Locate every leukocyte (white blood cell).
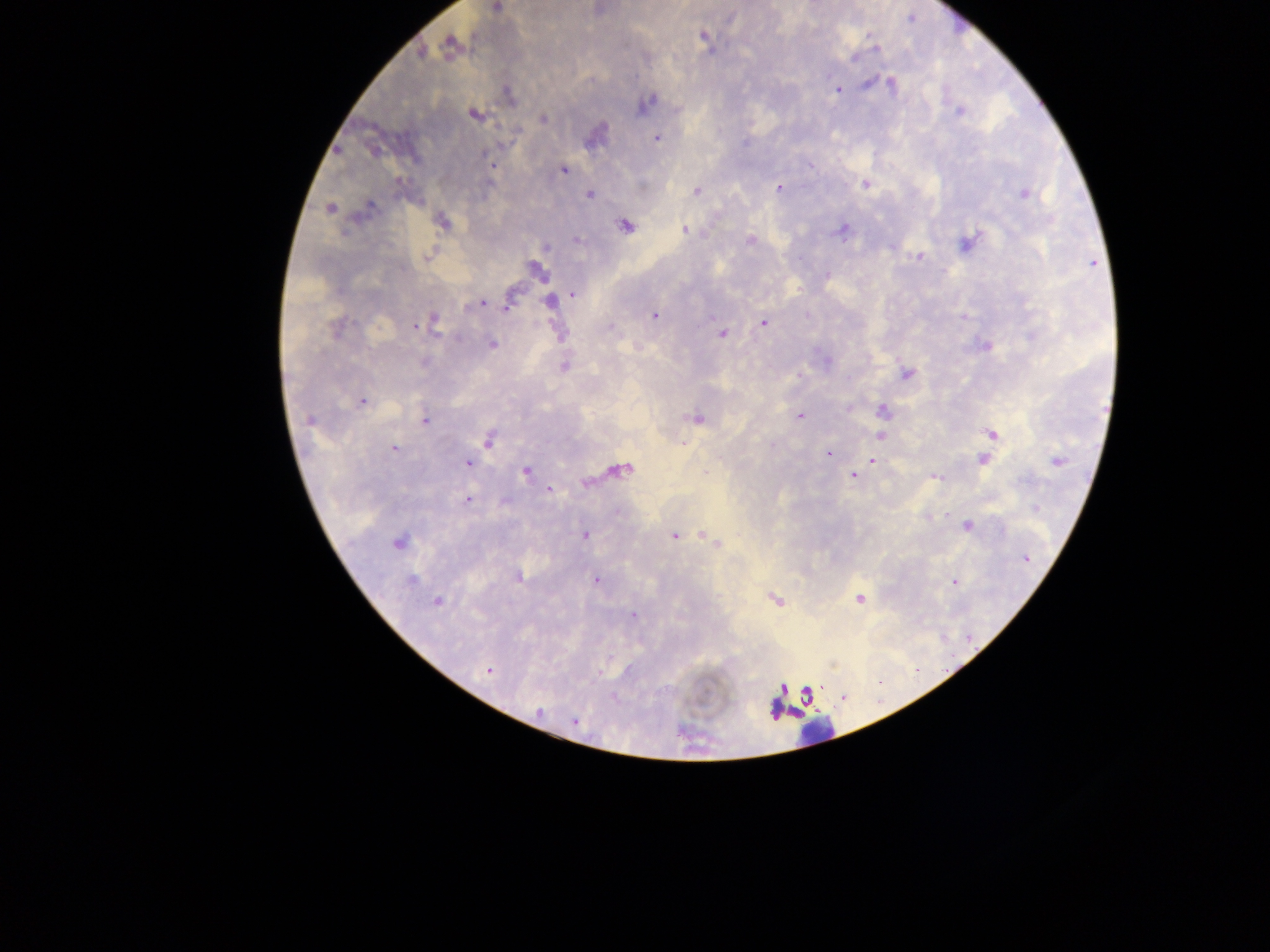

Approximate centers as (x, y) in pixels.
Leukocytes: (815, 732).

Plasmodium parasite locations: (495, 7), (703, 35), (450, 45), (875, 48), (891, 85), (837, 90), (508, 95), (646, 102), (959, 111), (474, 113), (543, 119), (595, 134), (656, 137), (492, 164), (562, 169), (866, 184), (779, 187), (696, 191), (589, 193), (1023, 193), (330, 208), (364, 210), (442, 221), (625, 225), (684, 229), (842, 231), (752, 239), (576, 240), (967, 242), (427, 256), (919, 257), (536, 271), (826, 275), (572, 294), (508, 302), (550, 302), (480, 303), (654, 315), (431, 321), (764, 323), (416, 325), (335, 328), (721, 333), (492, 344), (986, 345), (564, 366), (907, 374), (797, 375), (361, 401), (881, 410), (799, 415), (696, 418), (310, 420), (425, 421), (990, 433), (881, 434), (488, 438), (393, 449), (828, 454), (983, 460), (872, 461), (1057, 461), (468, 463), (619, 470), (525, 471), (857, 471), (853, 475), (934, 476), (548, 489), (468, 500), (967, 525), (584, 534), (702, 534), (674, 536), (398, 541), (718, 544), (518, 575), (411, 580), (597, 580), (954, 581), (774, 598), (860, 598), (437, 602), (632, 614), (487, 669), (574, 720). Single field of view. Collected in Ghana. Thick blood film. Image is 1270×952 pixels. Photographed through a microscope with a mobile-phone camera.